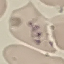

{
  "result": "no malaria parasites detected",
  "preparation": "thin blood smear",
  "stain": "Giemsa",
  "image_type": "cell patch, automatically extracted from a larger field of view and resized to 64 × 64 pixels",
  "capture": "smartphone through the microscope eyepiece"
}